Name the blood parasite species.
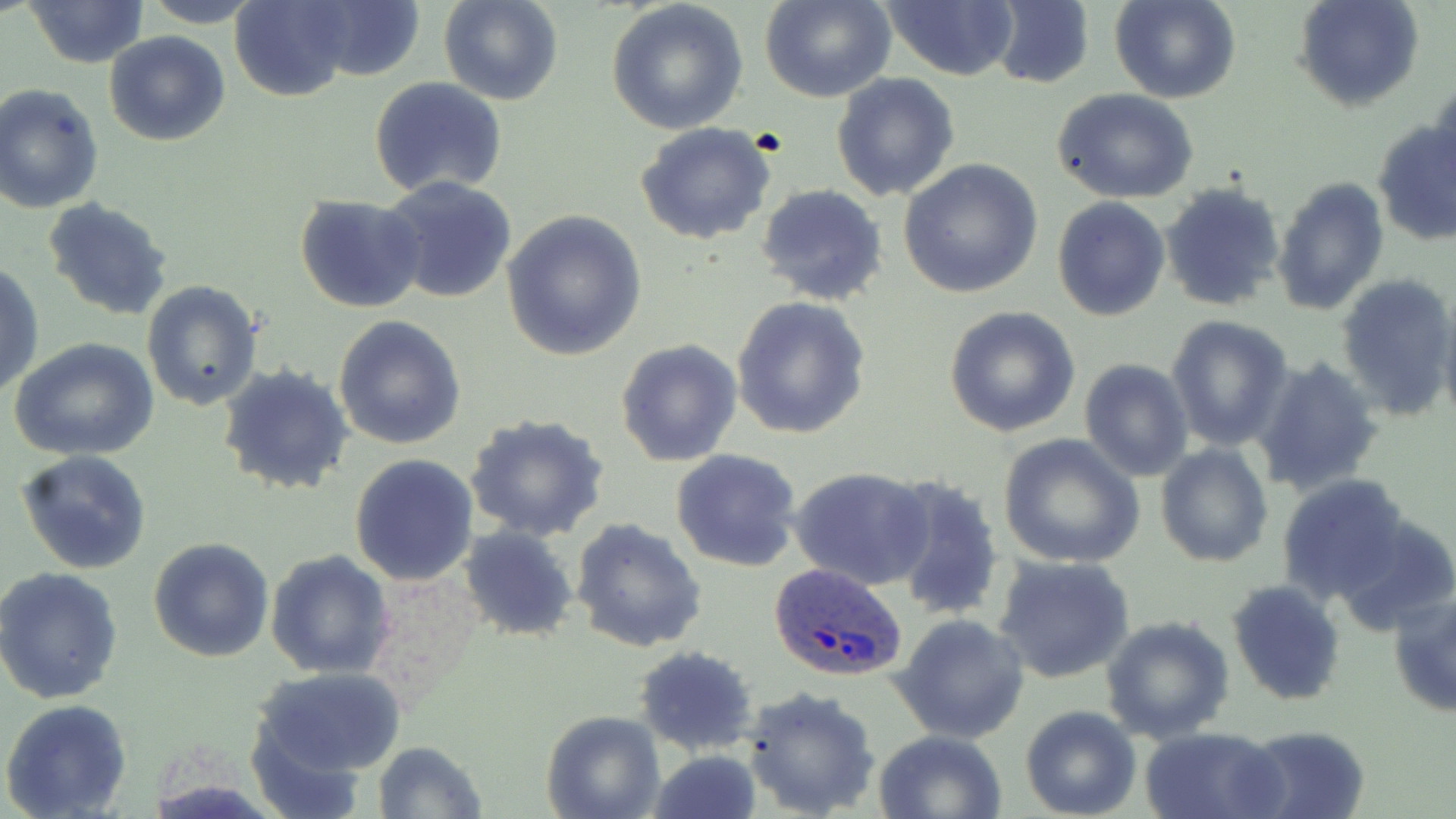
Plasmodium ovale.

Approximate bounding boxes as named x1/y1/x2/y2 corners in pixels. Uninfected red blood cell locations: (x1=139, y1=0, x2=267, y2=27), (x1=227, y1=0, x2=357, y2=102), (x1=437, y1=0, x2=564, y2=107), (x1=759, y1=0, x2=896, y2=103), (x1=1111, y1=0, x2=1239, y2=104), (x1=1295, y1=0, x2=1423, y2=112), (x1=25, y1=1, x2=148, y2=68), (x1=295, y1=1, x2=428, y2=85), (x1=606, y1=1, x2=750, y2=136), (x1=883, y1=1, x2=1020, y2=81), (x1=989, y1=1, x2=1095, y2=89), (x1=104, y1=31, x2=232, y2=147), (x1=1433, y1=70, x2=1456, y2=177), (x1=831, y1=74, x2=961, y2=202), (x1=370, y1=77, x2=508, y2=198), (x1=0, y1=84, x2=104, y2=214), (x1=1053, y1=89, x2=1200, y2=204), (x1=1372, y1=119, x2=1456, y2=246), (x1=636, y1=123, x2=778, y2=246), (x1=899, y1=159, x2=1044, y2=300), (x1=380, y1=176, x2=516, y2=304), (x1=1273, y1=177, x2=1389, y2=315), (x1=1162, y1=182, x2=1285, y2=312), (x1=756, y1=184, x2=887, y2=306), (x1=295, y1=195, x2=426, y2=314), (x1=42, y1=196, x2=175, y2=321), (x1=1052, y1=198, x2=1170, y2=322), (x1=501, y1=212, x2=646, y2=360), (x1=1, y1=262, x2=44, y2=401), (x1=1335, y1=272, x2=1456, y2=419), (x1=142, y1=279, x2=264, y2=411), (x1=731, y1=296, x2=873, y2=440), (x1=1437, y1=298, x2=1456, y2=434), (x1=942, y1=305, x2=1080, y2=438), (x1=333, y1=315, x2=466, y2=449), (x1=1166, y1=315, x2=1294, y2=451), (x1=12, y1=339, x2=158, y2=462), (x1=615, y1=340, x2=741, y2=467), (x1=1253, y1=357, x2=1385, y2=496), (x1=1079, y1=359, x2=1193, y2=482), (x1=217, y1=364, x2=354, y2=498), (x1=462, y1=413, x2=610, y2=541), (x1=996, y1=435, x2=1144, y2=567), (x1=1155, y1=444, x2=1274, y2=567), (x1=670, y1=448, x2=803, y2=572), (x1=17, y1=451, x2=154, y2=573), (x1=349, y1=454, x2=479, y2=587), (x1=789, y1=465, x2=933, y2=590), (x1=1277, y1=473, x2=1413, y2=605), (x1=884, y1=475, x2=1005, y2=623), (x1=571, y1=518, x2=708, y2=653), (x1=460, y1=526, x2=578, y2=642), (x1=148, y1=538, x2=273, y2=662), (x1=266, y1=550, x2=395, y2=679), (x1=992, y1=554, x2=1136, y2=684), (x1=0, y1=568, x2=123, y2=704), (x1=1227, y1=581, x2=1346, y2=704), (x1=1388, y1=591, x2=1456, y2=719), (x1=893, y1=612, x2=1030, y2=744), (x1=1101, y1=614, x2=1236, y2=743), (x1=634, y1=647, x2=760, y2=756), (x1=251, y1=667, x2=410, y2=784), (x1=741, y1=685, x2=882, y2=818), (x1=1, y1=700, x2=133, y2=819), (x1=1019, y1=705, x2=1142, y2=819), (x1=542, y1=710, x2=664, y2=819), (x1=1238, y1=724, x2=1372, y2=819), (x1=1140, y1=727, x2=1285, y2=819), (x1=872, y1=729, x2=1008, y2=819), (x1=373, y1=741, x2=485, y2=818), (x1=650, y1=745, x2=762, y2=819). Plasmodium ovale-infected red blood cell locations: (x1=767, y1=563, x2=907, y2=683). Thin blood smear. Image is 1456×819 pixels. Captured at 1000x magnification. Light microscopy. May-Grünwald-Giemsa-stained preparation. Single field of view.